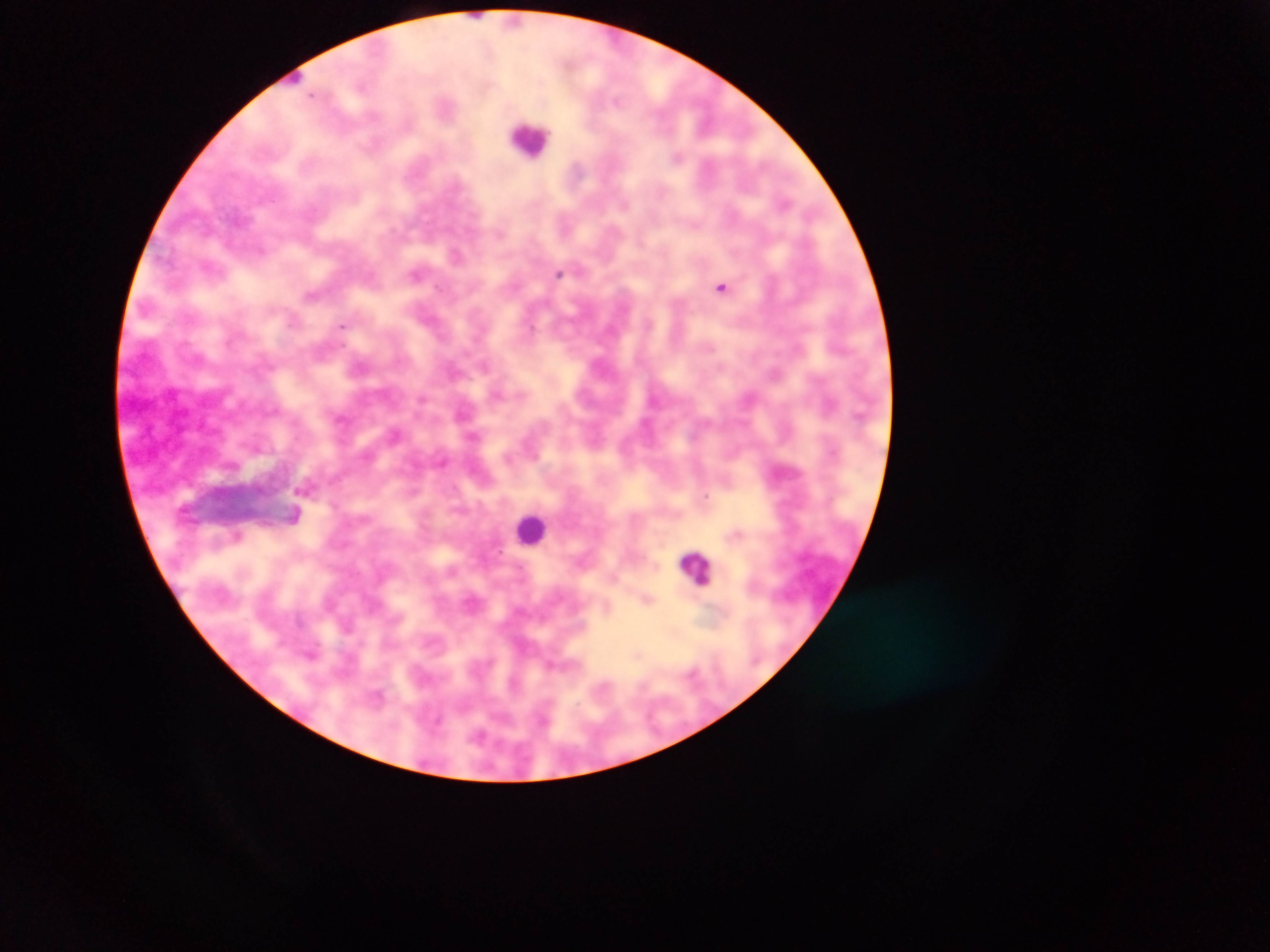
Approximate centers as [x, y] in pixels. Plasmodium parasite locations: [678, 157], [456, 254], [417, 273], [559, 273], [722, 286], [312, 296], [342, 326], [396, 434], [508, 458], [305, 488], [295, 515], [647, 600], [480, 735]. Leukocyte locations: [530, 138], [531, 529], [695, 567]. Mobile-phone photograph taken through the microscope. Single field of view. Thick blood smear. Image is 1270×952 pixels. Sample from Ghana.